Outline each Plasmodium malariae-infected red blood cell.
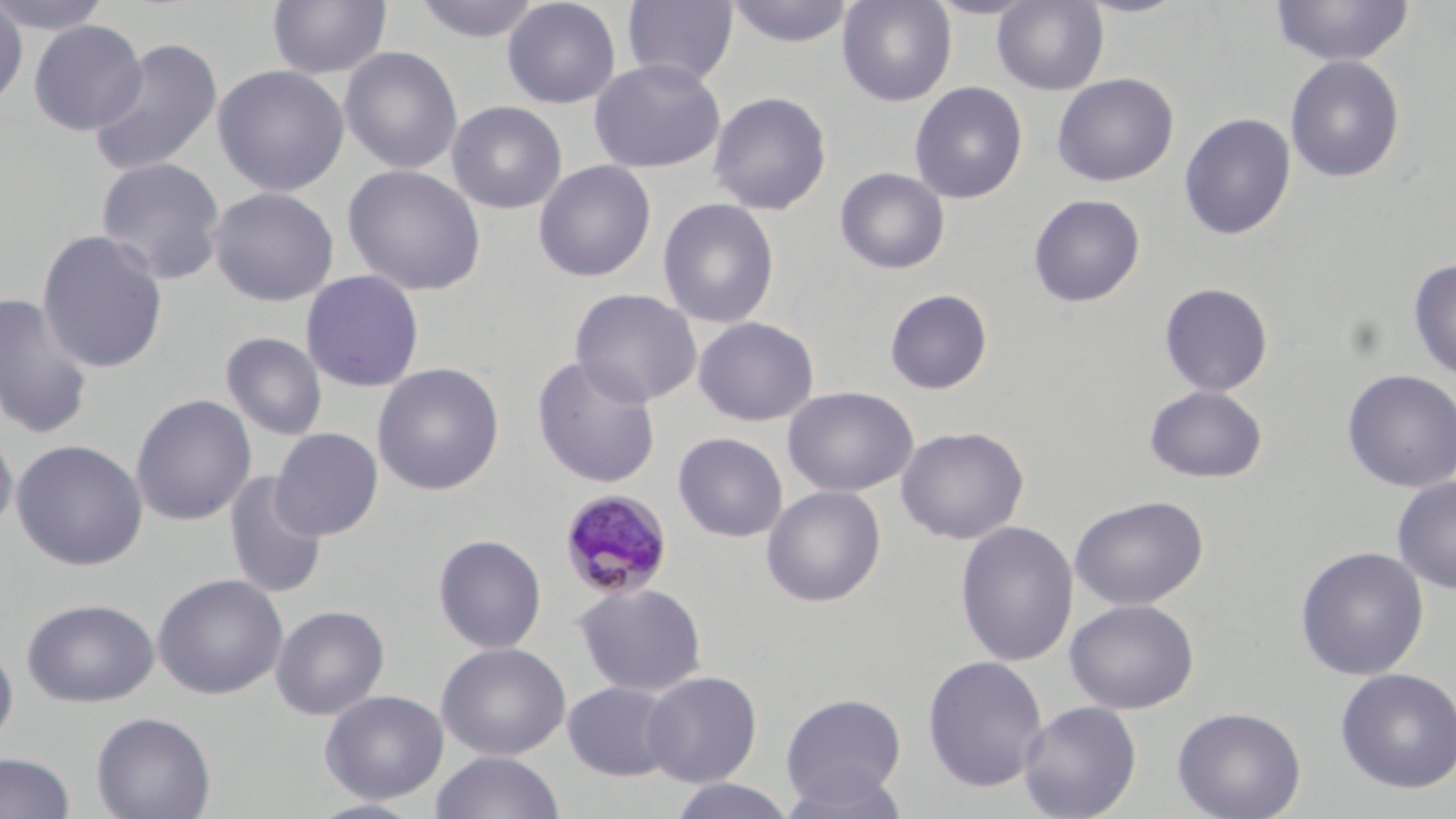
Approximate bounding boxes as (x1, y1, x2, y2) in pixels.
Plasmodium malariae-infected red blood cells: (558, 489, 674, 600).

slide-level diagnosis = Plasmodium malariae
image size = 1456×819 pixels
field of view = single
stain = May-Grünwald-Giemsa
magnification = 1000x
modality = optical microscopy
preparation = thin blood film
uninfected red blood cell locations = approximate bounding boxes as (x1, y1, x2, y2) in pixels: (0, 0, 115, 35), (267, 0, 392, 80), (412, 0, 542, 44), (502, 0, 622, 108), (622, 0, 738, 86), (837, 0, 957, 107), (992, 0, 1109, 95), (1074, 0, 1193, 18), (1271, 0, 1415, 66), (725, 1, 855, 48), (0, 2, 28, 110), (28, 20, 148, 136), (87, 38, 222, 177), (339, 46, 463, 175), (1285, 55, 1406, 182), (588, 58, 726, 173), (212, 64, 349, 197), (1052, 73, 1179, 187), (909, 81, 1028, 204), (708, 90, 832, 215), (447, 100, 567, 214), (1179, 113, 1296, 240), (95, 157, 227, 285), (533, 160, 656, 282), (342, 164, 486, 296), (835, 167, 950, 274), (207, 186, 339, 306), (1028, 194, 1146, 307), (657, 197, 780, 329), (37, 229, 169, 374), (1407, 259, 1456, 380), (300, 270, 425, 393), (1158, 282, 1274, 397), (570, 288, 702, 408), (884, 288, 994, 395), (0, 292, 95, 439), (693, 317, 818, 426), (220, 332, 328, 441), (531, 355, 661, 489), (372, 362, 505, 496), (1342, 369, 1456, 492), (1143, 385, 1269, 483), (783, 386, 919, 497), (130, 393, 257, 527), (0, 423, 18, 539), (896, 426, 1029, 544), (269, 428, 384, 541), (673, 432, 788, 542), (11, 438, 148, 571), (224, 472, 328, 599), (1392, 476, 1456, 594), (761, 485, 887, 607), (1070, 495, 1209, 611), (956, 521, 1078, 667), (433, 534, 547, 654), (1295, 546, 1429, 680), (152, 573, 288, 700), (572, 582, 707, 697), (21, 598, 159, 707), (1064, 598, 1199, 714), (270, 604, 390, 721), (0, 638, 18, 752), (436, 641, 571, 761), (922, 654, 1048, 792), (1335, 667, 1456, 793), (641, 670, 762, 787), (561, 680, 681, 782), (319, 689, 448, 804), (780, 692, 907, 809), (1017, 700, 1142, 819), (1171, 706, 1306, 819), (90, 711, 216, 819), (0, 751, 76, 819), (430, 751, 565, 819), (780, 766, 911, 819), (666, 778, 798, 819), (305, 798, 433, 819)